Assess this cell for malaria.
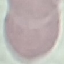

Uninfected.

Summary:
  - Capture: smartphone camera at the microscope eyepiece
  - Preparation: thin blood film
  - Image type: cell patch, automatically extracted from a larger field of view and resized to 64 × 64 pixels
  - Stain: Giemsa